Report the malaria status of this cell.
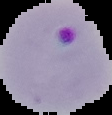

Parasitized.

image_size: 112×115 pixels
preparation: thin blood smear
image_type: cell region segmented out of the field of view; surrounding area masked to black